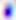

Summary:
  - Modality: micrograph
  - Magnification: 400x
  - Identification: Toxoplasma gondii